Assess this cell for malaria.
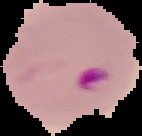

Parasitized.

From a thin blood film. Segmented cell region on a black background. Image is 142×136 pixels.